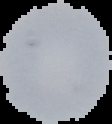

preparation = thin blood smear
image type = cell region segmented out of the field of view; surrounding area masked to black
image size = 112×124 pixels
result = no malaria parasites seen